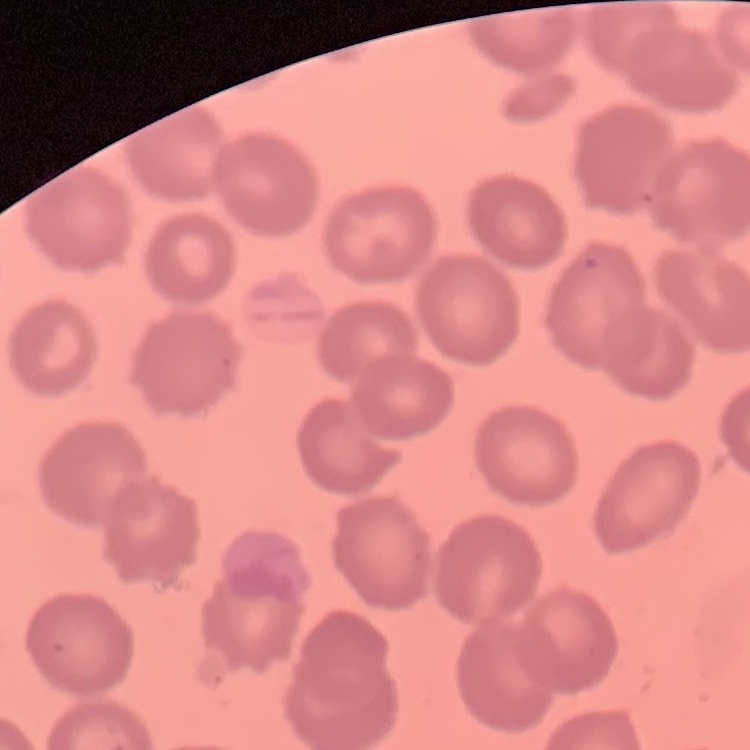
Summary:
  - Red blood cell morphology: no rouleaux formation
  - Preparation: thin blood film
  - Image type: one tile cut from a larger photomicrograph
  - Stain: Field's or Giemsa